Name the parasite shown.
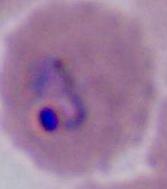

Plasmodium.

{
  "modality": "micrograph",
  "magnification": "400x or 1000x"
}